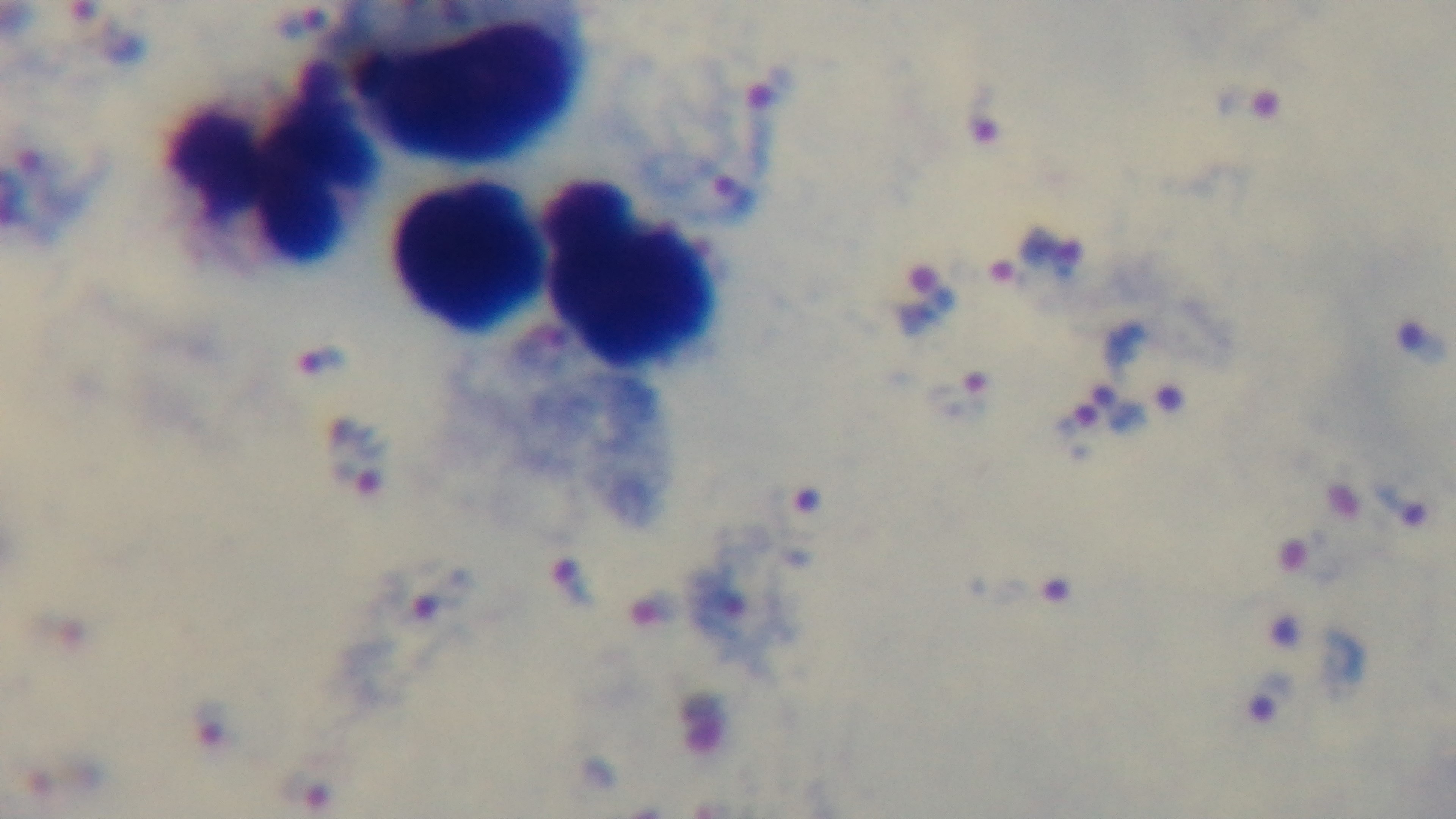
capture = mounted 4K digital camera
field of view = single
modality = light microscopy
objective = 100x oil immersion
preparation = thick smear
malaria status = infected
stain = Giemsa